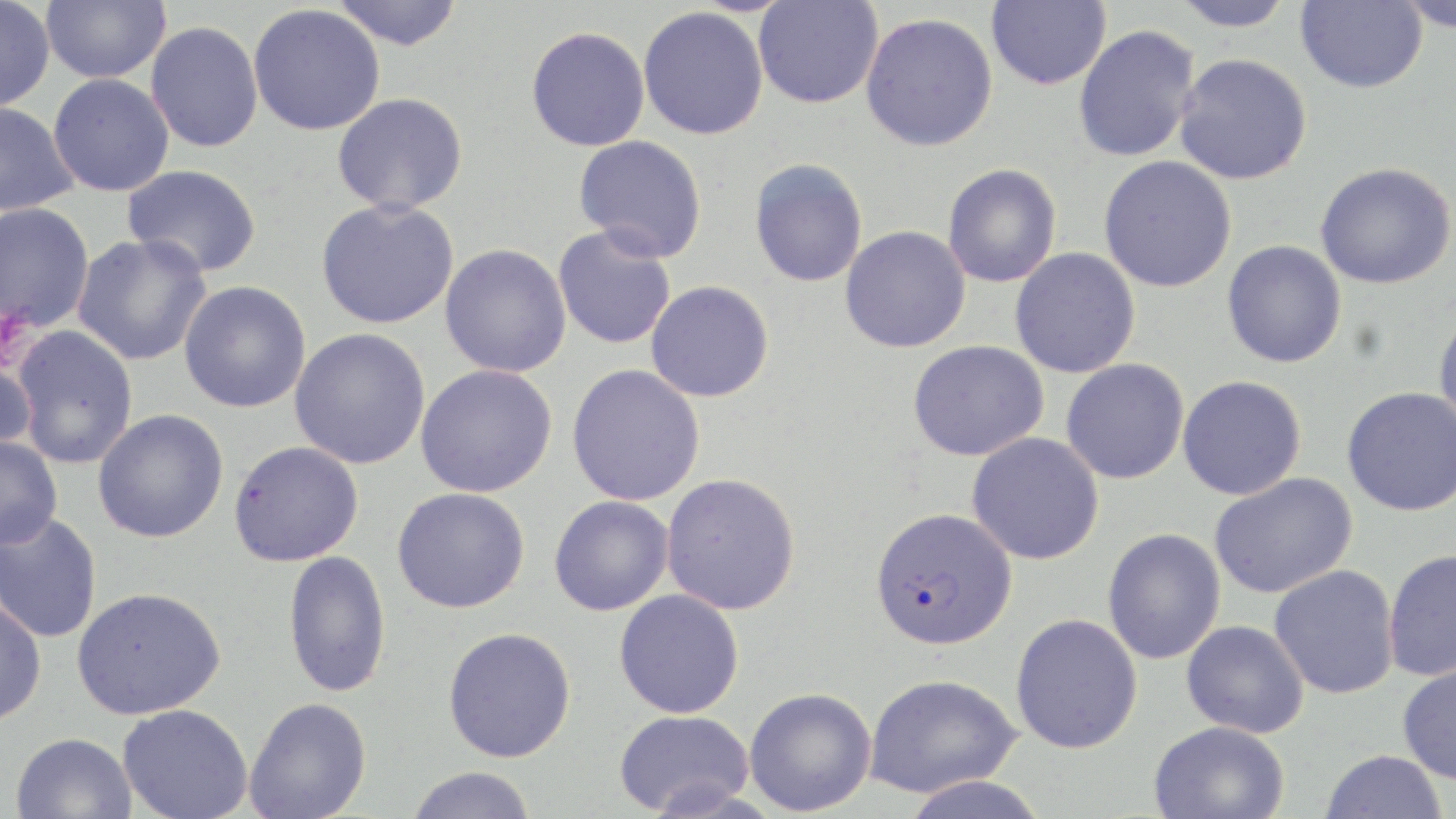

slide_level_diagnosis: Plasmodium falciparum
image_size: 1456×819 pixels
platelet_locations: 'approximate bounding boxes as (x1,y1)-(x2,y2) corner pairs in pixels: (0,304)-(36,372)'
plasmodium_falciparum_infected_red_blood_cell_locations: 'approximate bounding boxes as (x1,y1)-(x2,y2) corner pairs in pixels: (870,507)-(1017,650)'
field_of_view: one of a larger specimen
modality: optical microscopy
magnification: 1000x
preparation: thin blood film
stain: May-Grünwald-Giemsa
uninfected_red_blood_cell_locations: 'approximate bounding boxes as (x1,y1)-(x2,y2) corner pairs in pixels: (330,0)-(464,51), (753,0)-(883,109), (987,0)-(1111,90), (1170,0)-(1297,31), (1296,0)-(1428,93), (0,1)-(55,111), (41,1)-(170,83), (1397,1)-(1456,31), (247,5)-(386,136), (638,6)-(769,140), (860,12)-(998,152), (146,21)-(263,152), (1073,24)-(1200,163), (526,26)-(650,152), (1174,53)-(1312,185), (48,73)-(175,196), (332,92)-(468,214), (0,101)-(79,216), (572,134)-(708,261), (1098,155)-(1236,293), (749,159)-(868,288), (1315,162)-(1455,289), (122,164)-(262,277), (942,164)-(1062,288), (316,198)-(460,330), (0,202)-(95,332), (552,225)-(678,350), (840,225)-(970,353), (72,234)-(211,366), (1222,240)-(1347,368), (440,243)-(572,378), (1010,248)-(1141,378), (645,280)-(774,402), (179,281)-(311,413), (1433,309)-(1456,439), (11,326)-(139,468), (289,328)-(431,469), (907,340)-(1049,461), (0,351)-(37,459), (1061,358)-(1189,485), (415,364)-(557,497), (567,364)-(705,506), (1178,375)-(1306,500), (1341,387)-(1456,516), (93,409)-(228,543), (966,432)-(1104,565), (0,435)-(63,550), (228,440)-(364,567), (661,472)-(801,615), (1209,472)-(1357,599), (392,487)-(531,613), (549,495)-(674,615), (0,512)-(103,643), (1102,528)-(1226,665), (1382,548)-(1456,682), (283,550)-(391,698), (1268,565)-(1400,700), (72,586)-(225,719), (614,589)-(744,718), (0,592)-(47,726), (1011,613)-(1143,754), (1181,620)-(1309,738), (442,627)-(577,763), (1397,660)-(1456,785), (864,673)-(1021,799), (744,687)-(876,816), (244,697)-(372,819), (117,704)-(253,819), (613,710)-(754,815), (1148,721)-(1290,819), (10,732)-(137,819), (1320,749)-(1447,819), (405,766)-(538,819)'